Report the malaria status of this cell.
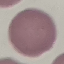

It is uninfected.

Summary:
  - Stain: Giemsa
  - Preparation: thin smear
  - Image type: cell patch, automatically extracted from a larger field of view and resized to 64 × 64 pixels
  - Capture: smartphone camera at the microscope eyepiece